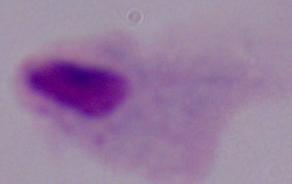
A trichomonad is shown. Captured at 1000x magnification. Micrograph.